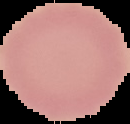
Summary:
  - Image type: segmented cell region with the area outside set to black
  - Result: no malaria parasites seen
  - Preparation: thin blood film
  - Image size: 130×124 pixels